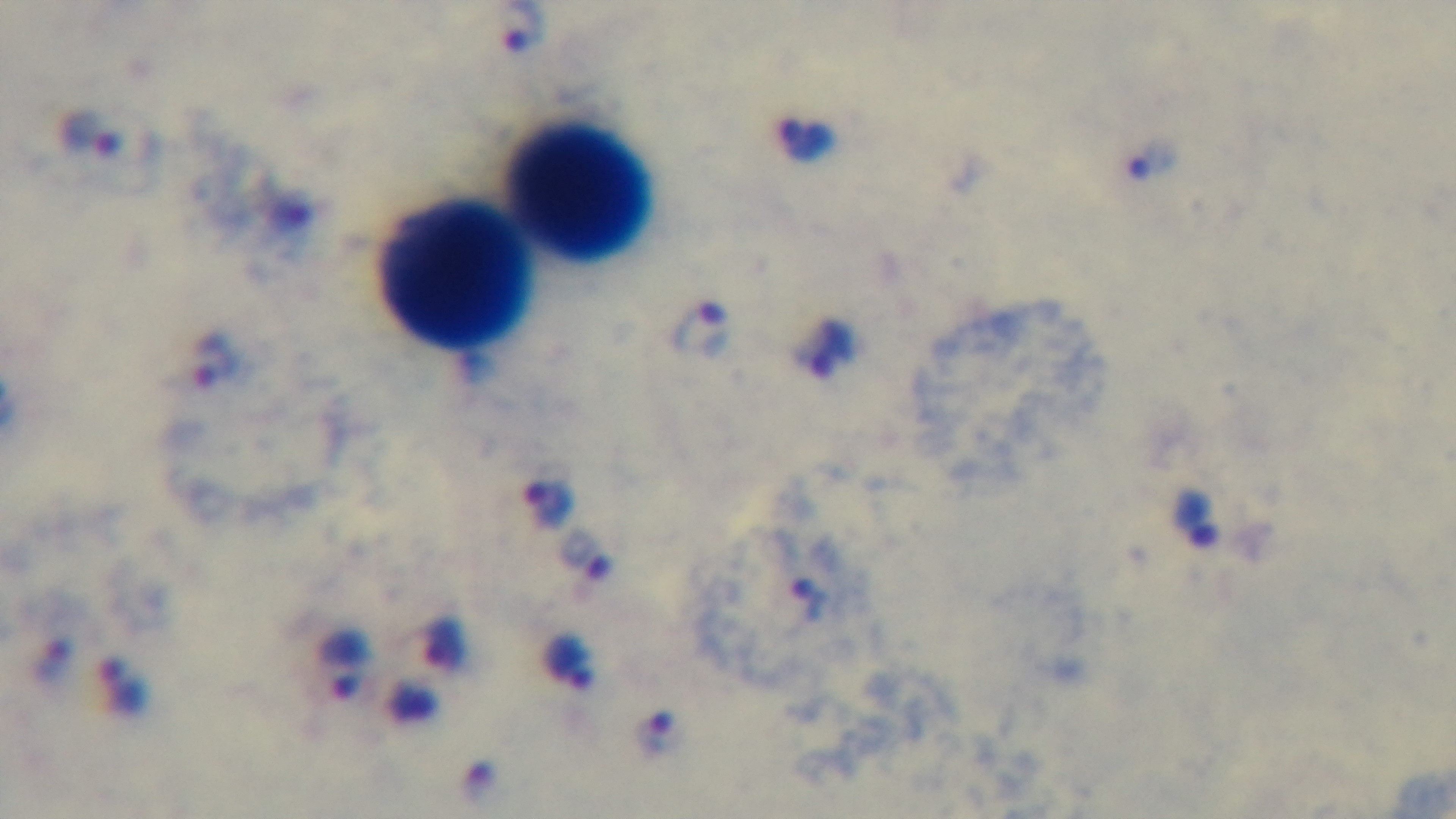
modality = light microscopy
field of view = single
objective = 100x oil immersion
stain = Giemsa
preparation = thick
malaria status = positive
capture = mounted 4K digital camera